Classify this cell by malaria status.
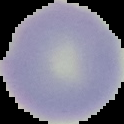

It is uninfected.

Summary:
  - Preparation: thin blood film
  - Image type: segmented cell region with the area outside set to black
  - Image size: 124×124 pixels